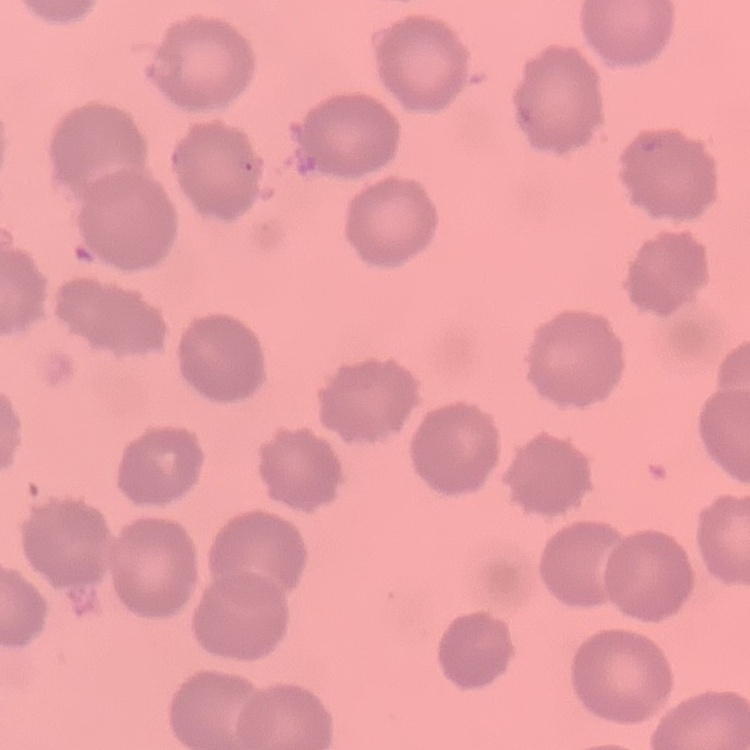
The red blood cells exhibit no rouleaux formation. One tile cut from a larger photomicrograph. Thin blood smear. Stained with either Field's or Giemsa.